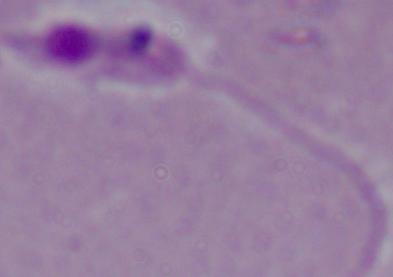
magnification = 1000x
identification = Leishmania
modality = photomicrograph